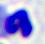

Summary:
  - Magnification: 400x
  - Modality: micrograph
  - Identification: white blood cell